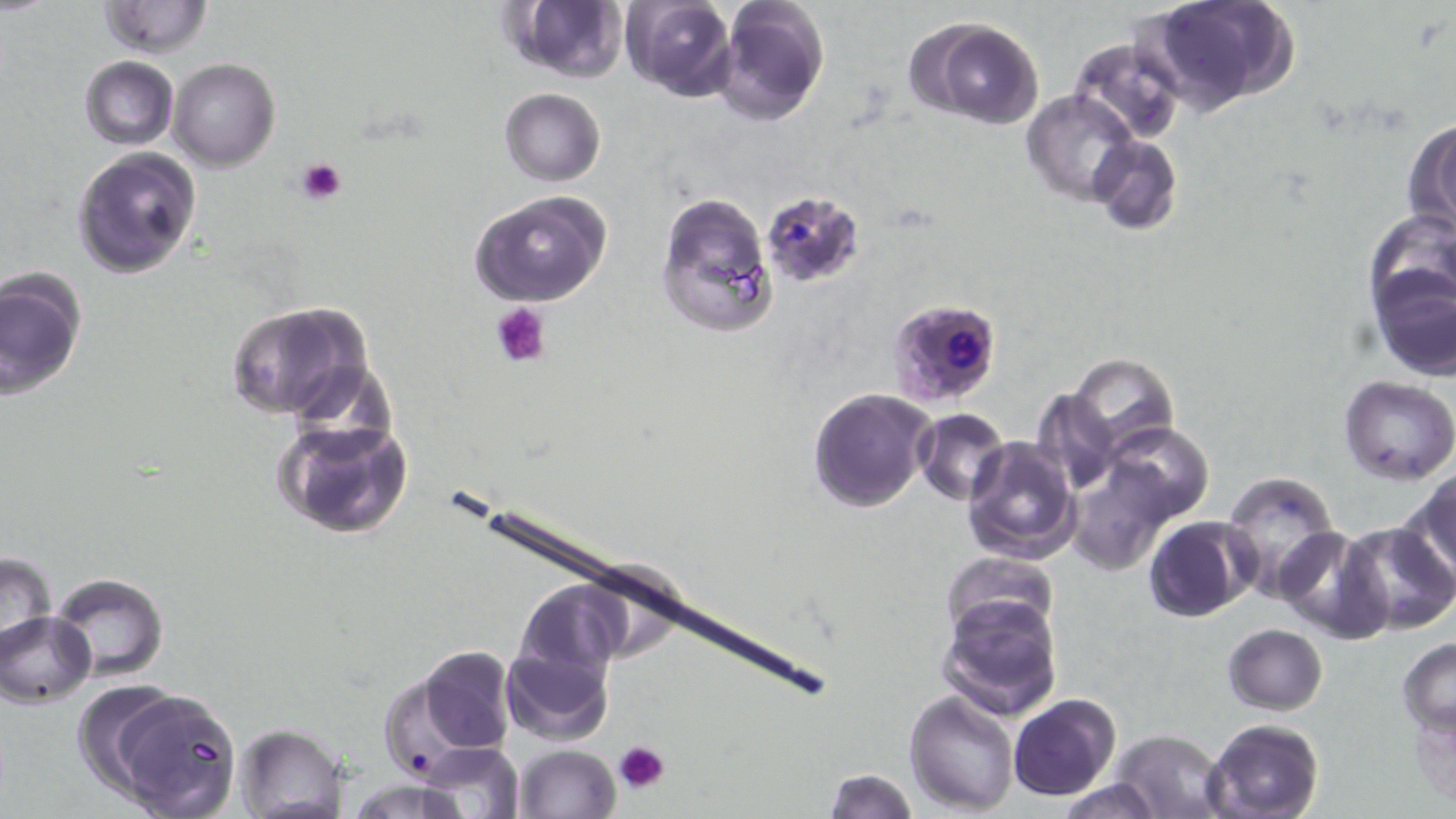
Approximate bounding boxes as (x1, y1, x2, y2) in pixels. Plasmodium falciparum-infected red blood cell locations: (758, 192, 865, 290), (885, 295, 1004, 408). Uninfected red blood cell locations: (712, 0, 830, 125), (1141, 0, 1296, 110), (99, 1, 212, 58), (503, 1, 627, 83), (620, 1, 738, 100), (913, 19, 1044, 129), (1066, 34, 1185, 148), (78, 56, 179, 149), (169, 58, 280, 171), (498, 88, 605, 187), (1023, 90, 1140, 206), (1403, 119, 1456, 239), (1087, 135, 1181, 235), (71, 147, 202, 279), (469, 190, 613, 308), (654, 190, 778, 340), (1365, 215, 1456, 325), (1369, 268, 1456, 381), (0, 269, 86, 400), (227, 300, 373, 422), (1069, 353, 1179, 453), (1338, 377, 1456, 483), (807, 387, 936, 514), (1030, 387, 1122, 495), (914, 408, 1011, 506), (270, 416, 415, 541), (1102, 424, 1214, 525), (962, 438, 1080, 564), (1067, 459, 1178, 573), (1221, 470, 1343, 598), (1400, 470, 1456, 586), (1143, 515, 1254, 623), (1336, 521, 1456, 636), (1275, 528, 1389, 643), (1, 550, 59, 658), (941, 551, 1060, 646), (597, 557, 688, 648), (52, 574, 166, 682), (530, 578, 638, 674), (938, 591, 1064, 720), (1, 612, 95, 706), (1223, 624, 1327, 715), (501, 630, 618, 747), (1397, 637, 1456, 736), (397, 645, 517, 769), (80, 680, 245, 817), (905, 690, 1019, 815), (1009, 694, 1119, 801), (1410, 698, 1456, 809), (1203, 718, 1325, 819), (234, 723, 351, 818), (1110, 728, 1230, 819), (415, 741, 526, 819), (512, 744, 621, 819), (824, 769, 918, 818), (1053, 777, 1163, 818). Platelet locations: (296, 156, 347, 204), (488, 300, 551, 367), (613, 739, 671, 794). Slide-level diagnosis: Plasmodium falciparum. Single field of view. Image is 1456×819 pixels. Light microscopy. Thin blood film. May-Grünwald-Giemsa stain. Captured at 1000x magnification.